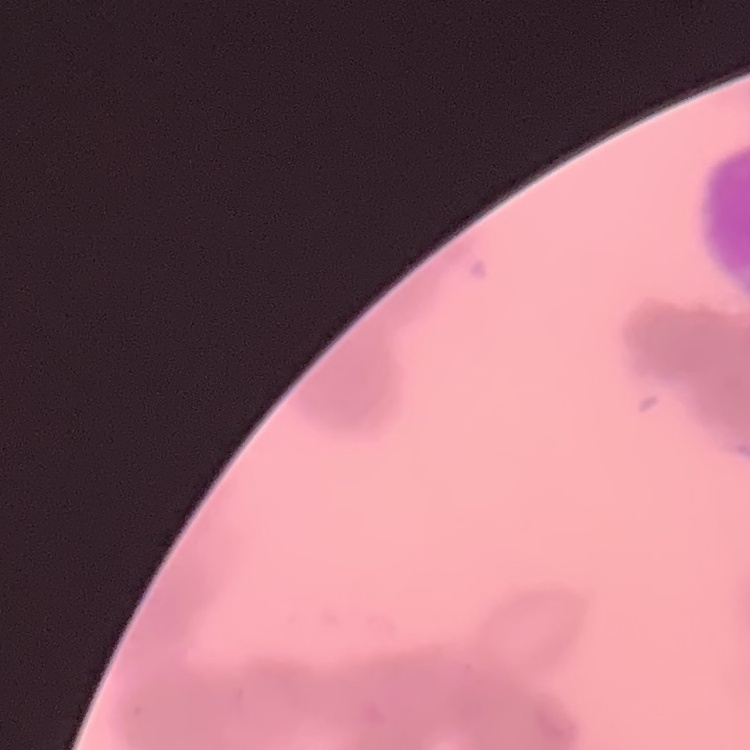
erythrocyte morphology = rouleaux formation
preparation = thin blood smear
stain = Field's or Giemsa
image type = square crop of a larger photomicrograph